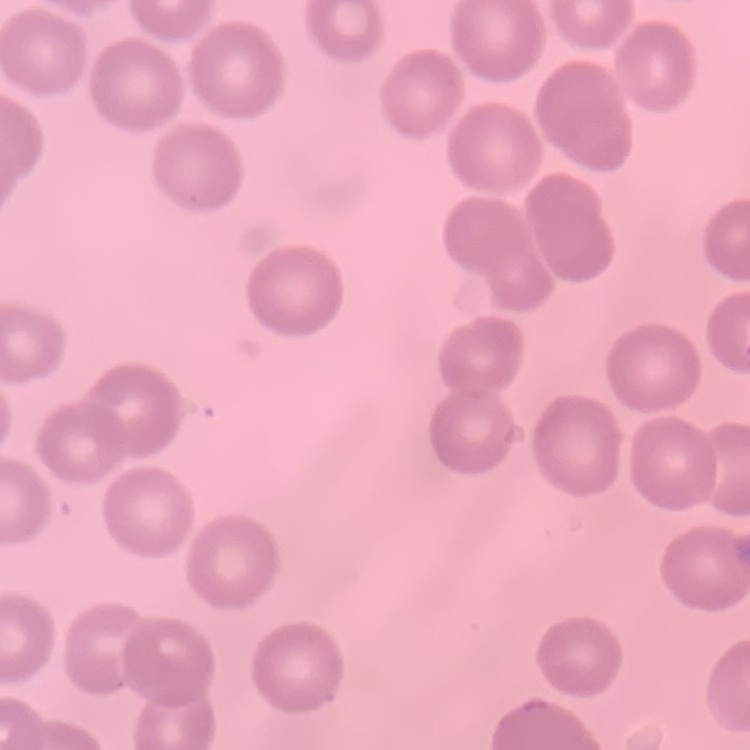

Summary:
  - Erythrocyte morphology: no rouleaux formation
  - Stain: Field's or Giemsa
  - Preparation: thin peripheral smear
  - Image type: one tile cut from a larger photomicrograph